Locate every Plasmodium parasite.
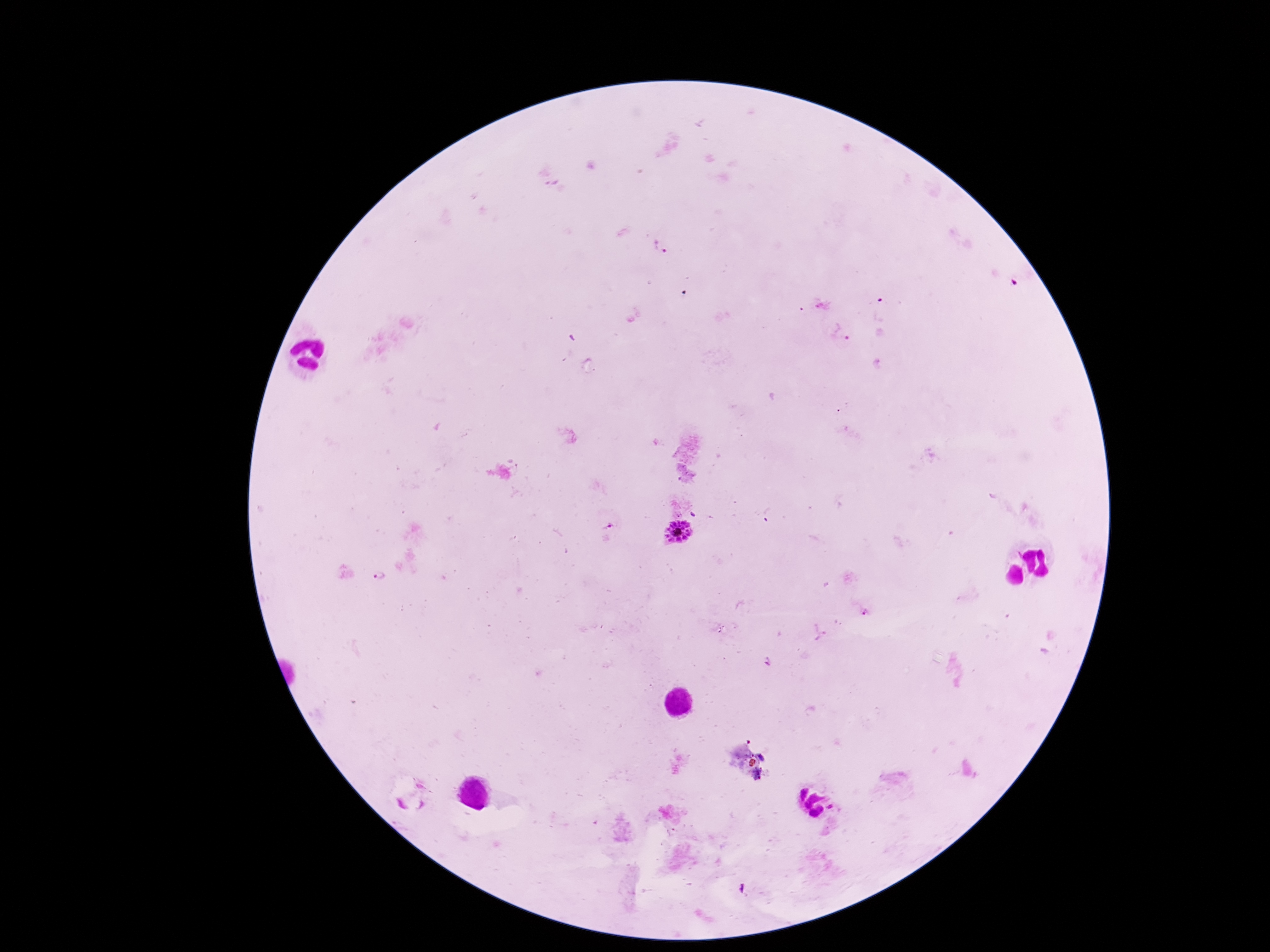

Approximate object centers, in pixels from the top-left corner.
Plasmodium parasites: (x=658, y=247), (x=841, y=333), (x=680, y=536), (x=865, y=611).

100x magnification. Giemsa stain. Patient malaria status: positive. Photographed through the microscope eyepiece with a smartphone camera. Thick blood film. Image is 1270×952 pixels. Single field of view.